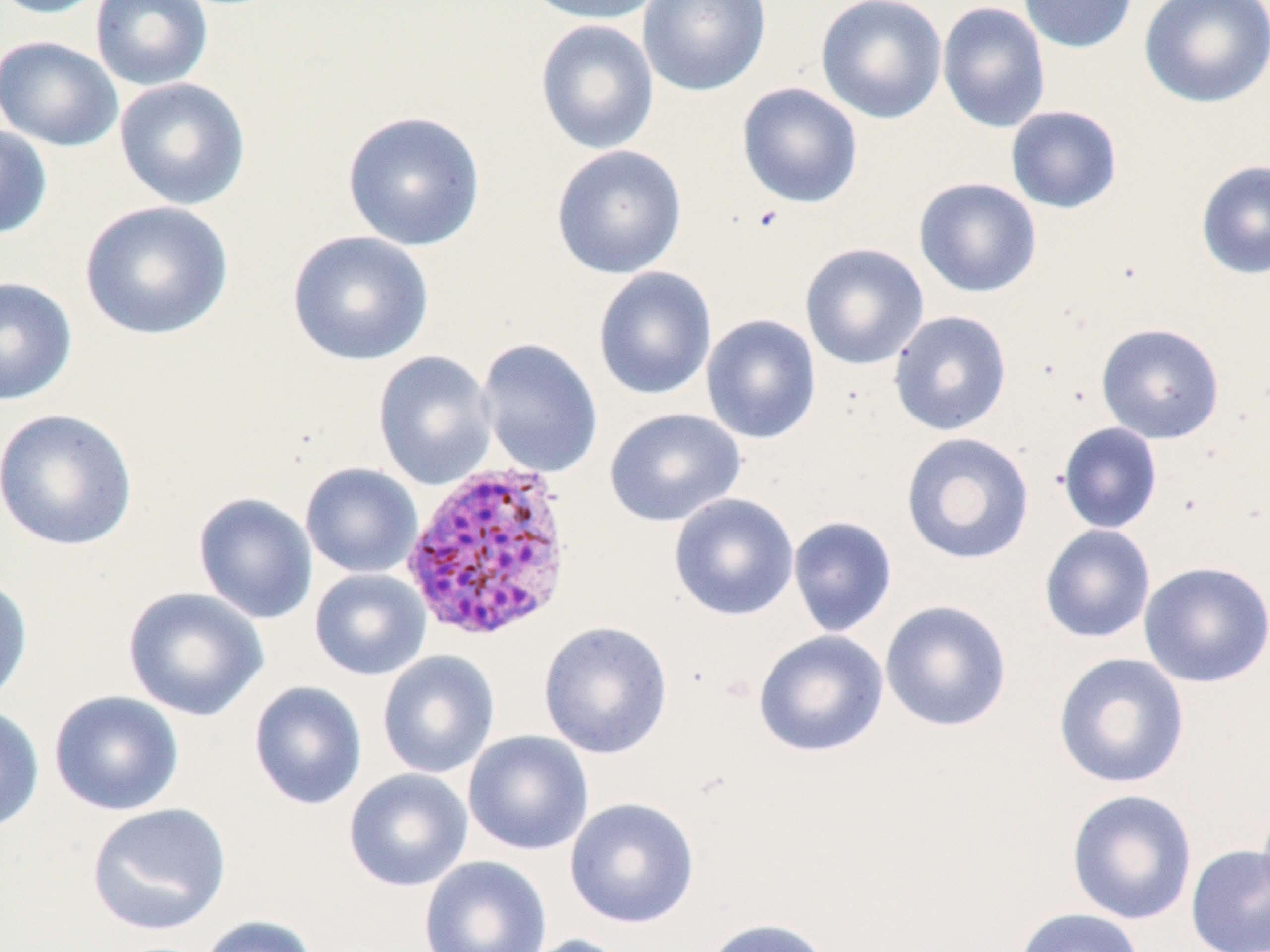
Summary:
  - Coordinate format: approximate bounding boxes as (x1, y1, x2, y2) in pixels
  - Plasmodium vivax-infected red blood cell locations: (399, 459, 576, 643)
  - Uninfected red blood cell locations: (0, 0, 109, 19), (90, 0, 214, 91), (520, 0, 664, 25), (638, 0, 771, 97), (815, 0, 948, 124), (1018, 0, 1138, 54), (1139, 0, 1270, 108), (937, 1, 1051, 134), (535, 19, 660, 155), (0, 35, 123, 152), (113, 77, 251, 211), (736, 82, 863, 209), (1005, 105, 1123, 214), (342, 110, 486, 251), (0, 124, 53, 240), (550, 144, 688, 280), (1195, 159, 1270, 280), (913, 177, 1042, 298), (79, 200, 234, 342), (287, 230, 434, 366), (799, 242, 929, 370), (593, 266, 717, 401), (0, 275, 78, 406), (888, 310, 1012, 436), (701, 314, 822, 445), (1095, 322, 1225, 444), (476, 338, 604, 478), (372, 351, 498, 490), (0, 407, 139, 552), (604, 407, 746, 528), (1056, 422, 1163, 534), (900, 432, 1035, 566), (300, 462, 423, 578), (193, 492, 319, 624), (668, 493, 800, 621), (787, 515, 897, 637), (1038, 524, 1156, 644), (1138, 560, 1270, 688), (309, 568, 431, 681), (0, 573, 33, 709), (122, 586, 269, 722), (879, 599, 1012, 733), (538, 620, 674, 759), (753, 630, 889, 758), (377, 651, 500, 779), (1052, 652, 1190, 790), (248, 681, 368, 811), (48, 690, 185, 816), (0, 704, 45, 834), (463, 730, 594, 857), (344, 768, 474, 891), (1065, 789, 1198, 925), (565, 796, 700, 928), (86, 802, 232, 935), (1185, 843, 1270, 951), (418, 855, 552, 952), (1013, 907, 1145, 952), (197, 915, 318, 952), (699, 917, 834, 952), (515, 933, 632, 952)
  - Slide-level diagnosis: Plasmodium vivax
  - Preparation: thin blood film
  - Modality: optical microscopy
  - Stain: May-Grünwald-Giemsa
  - Image size: 1270×952 pixels
  - Magnification: 1000x
  - Field of view: single